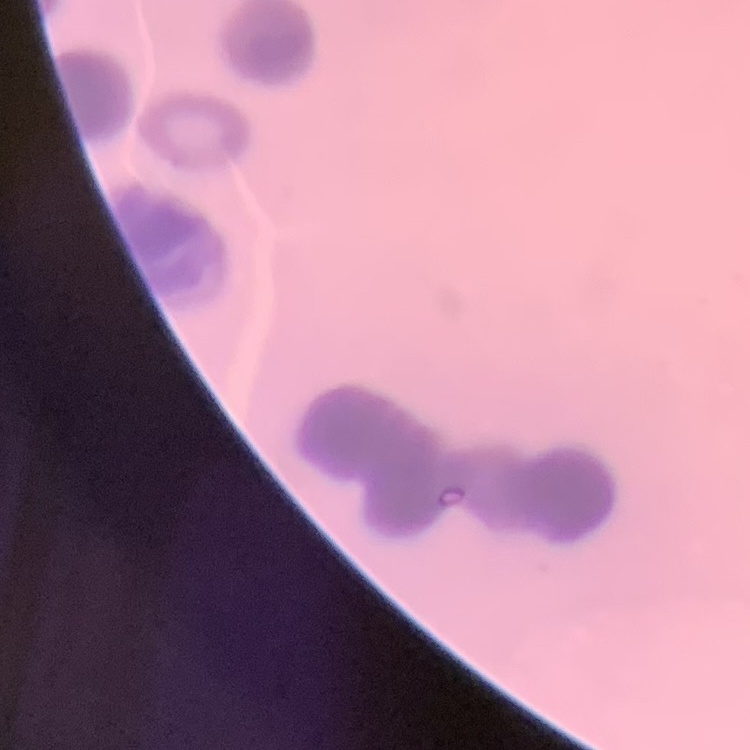
red_blood_cell_morphology: rouleaux formation
stain: Field's or Giemsa
image_type: square crop of a larger photomicrograph
preparation: thin blood smear